Outline platelets.
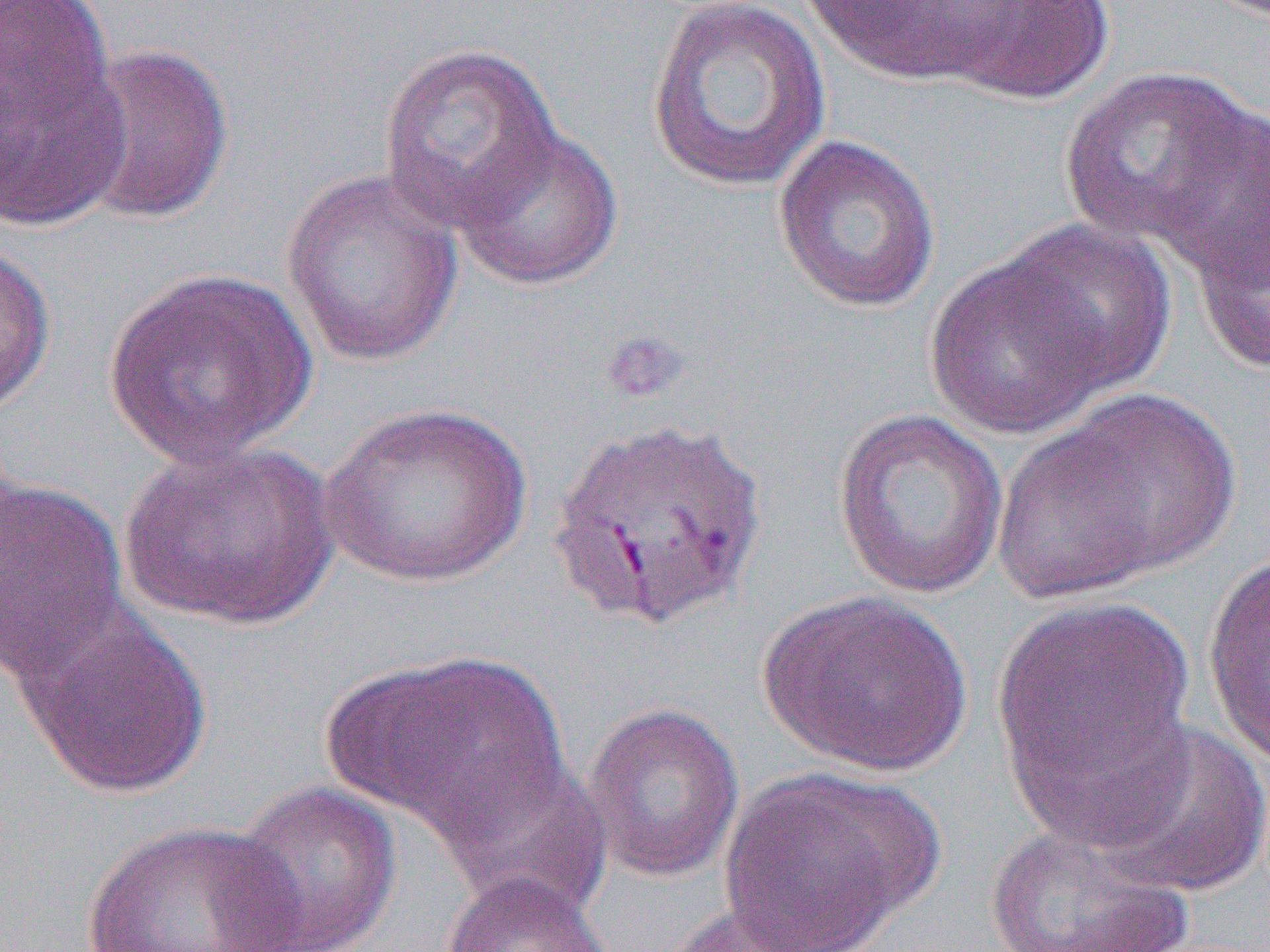
Approximate bounding boxes as (x1, y1, x2, y2) in pixels.
Platelets: (599, 328, 691, 405).

slide-level diagnosis = Plasmodium vivax
modality = light microscopy
preparation = thin blood film
uninfected red blood cell locations = approximate bounding boxes as (x1, y1, x2, y2) in pixels: (0, 0, 120, 146), (644, 0, 832, 193), (797, 0, 1028, 86), (932, 0, 1119, 104), (0, 30, 131, 237), (70, 41, 236, 227), (376, 41, 564, 234), (1059, 63, 1263, 259), (1156, 111, 1270, 307), (452, 123, 624, 291), (772, 134, 941, 313), (280, 168, 464, 368), (1190, 193, 1270, 381), (1001, 219, 1178, 397), (0, 241, 56, 418), (923, 252, 1113, 440), (103, 266, 318, 468), (1028, 384, 1244, 590), (319, 401, 531, 589), (832, 407, 1010, 600), (119, 440, 339, 631), (0, 472, 131, 685), (1201, 551, 1269, 770), (758, 590, 974, 778), (994, 594, 1196, 815), (9, 595, 213, 799), (342, 651, 572, 845), (582, 703, 746, 883), (1094, 721, 1270, 899), (437, 761, 616, 916), (718, 769, 932, 949), (225, 781, 402, 952), (79, 821, 306, 952), (981, 822, 1197, 951), (440, 870, 613, 952), (659, 901, 836, 952)
magnification = 1000x
image size = 1270×952 pixels
field of view = single